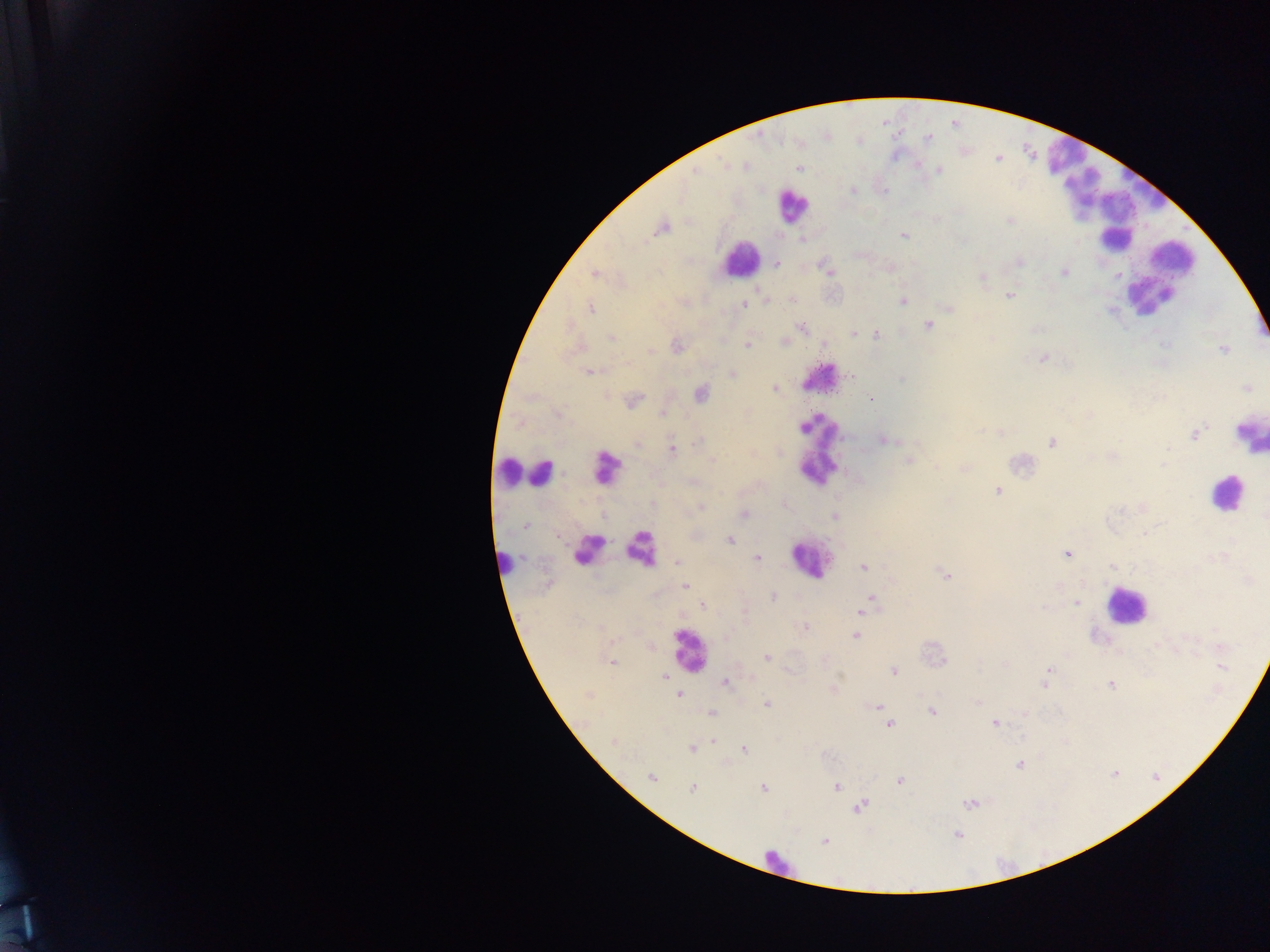
{
  "preparation": "thick blood smear",
  "field_of_view": "single",
  "malaria_parasite_locations": "approximate centers as {x, y} in pixels: {929, 138}, {724, 165}, {799, 168}, {695, 171}, {939, 171}, {853, 191}, {1010, 222}, {662, 228}, {904, 236}, {803, 239}, {1019, 262}, {777, 263}, {828, 272}, {1065, 272}, {595, 274}, {982, 278}, {1009, 296}, {792, 299}, {766, 300}, {903, 301}, {744, 305}, {949, 307}, {590, 309}, {928, 325}, {801, 327}, {853, 333}, {877, 335}, {611, 338}, {784, 342}, {747, 346}, {677, 347}, {1224, 349}, {651, 351}, {1044, 358}, {589, 372}, {732, 373}, {851, 375}, {901, 379}, {1246, 388}, {774, 389}, {700, 393}, {871, 400}, {635, 401}, {663, 414}, {1194, 435}, {886, 441}, {698, 442}, {1051, 442}, {636, 444}, {672, 449}, {1113, 457}, {712, 461}, {908, 461}, {1163, 465}, {964, 468}, {998, 491}, {784, 506}, {700, 507}, {1121, 508}, {743, 514}, {835, 517}, {525, 525}, {1144, 533}, {730, 541}, {1066, 554}, {757, 558}, {677, 561}, {1113, 566}, {863, 567}, {945, 575}, {685, 586}, {773, 597}, {872, 598}, {1076, 603}, {702, 606}, {867, 606}, {861, 612}, {805, 627}, {856, 636}, {767, 657}, {613, 663}, {1004, 665}, {1222, 667}, {1048, 670}, {894, 671}, {665, 677}, {1047, 677}, {725, 683}, {1044, 683}, {1111, 684}, {680, 695}, {978, 702}, {766, 704}, {875, 706}, {932, 712}, {711, 713}, {1026, 713}, {889, 724}, {995, 724}, {713, 741}, {614, 742}, {692, 749}, {743, 749}, {1019, 764}, {652, 778}, {900, 780}, {836, 786}, {763, 787}, {692, 788}, {968, 803}, {860, 806}, {824, 841}",
  "leukocyte_locations": "approximate centers as {x, y} in pixels: {1060, 150}, {1138, 189}, {791, 206}, {1100, 206}, {740, 259}, {1151, 280}, {819, 374}, {1249, 433}, {819, 448}, {607, 468}, {511, 470}, {542, 474}, {1224, 494}, {640, 545}, {582, 548}, {809, 561}, {504, 562}, {1125, 606}, {688, 650}, {779, 865}",
  "country": "Ghana",
  "image_size": "1270×952 pixels",
  "capture": "mobile-phone photograph through a microscope"
}